Give the extent of all uninfected red blood cells.
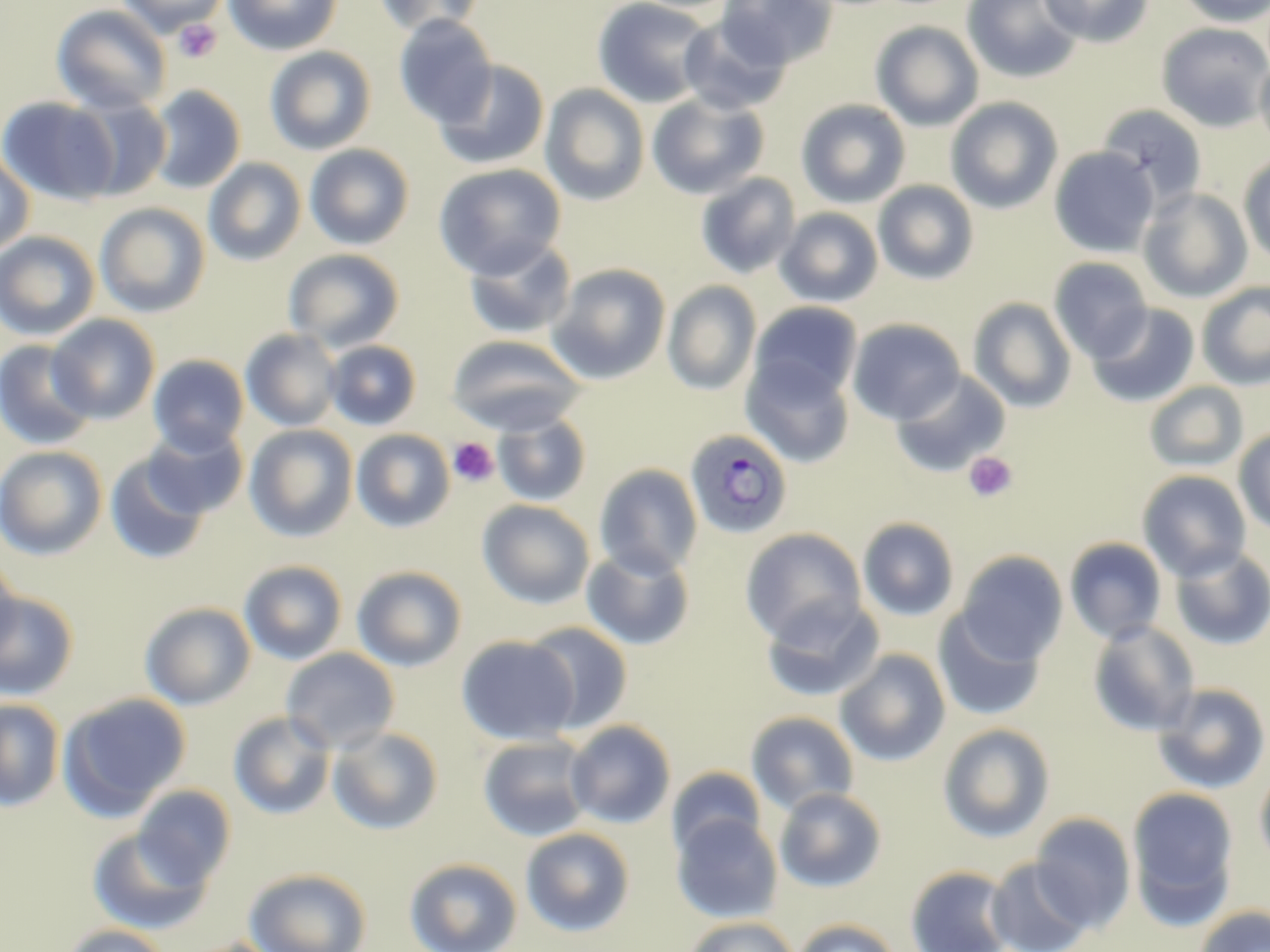
Approximate bounding boxes as named x1/y1/x2/y2 corners in pixels.
Uninfected red blood cells: (x1=115, y1=0, x2=229, y2=35), (x1=223, y1=0, x2=341, y2=56), (x1=373, y1=0, x2=486, y2=37), (x1=592, y1=0, x2=714, y2=109), (x1=717, y1=0, x2=837, y2=70), (x1=962, y1=0, x2=1083, y2=83), (x1=1039, y1=0, x2=1154, y2=47), (x1=1178, y1=0, x2=1270, y2=27), (x1=51, y1=4, x2=172, y2=115), (x1=393, y1=15, x2=498, y2=129), (x1=678, y1=17, x2=791, y2=115), (x1=871, y1=21, x2=984, y2=131), (x1=1156, y1=23, x2=1270, y2=131), (x1=264, y1=46, x2=376, y2=155), (x1=1255, y1=58, x2=1270, y2=154), (x1=433, y1=60, x2=550, y2=170), (x1=541, y1=84, x2=650, y2=206), (x1=148, y1=85, x2=245, y2=194), (x1=647, y1=93, x2=769, y2=200), (x1=0, y1=97, x2=121, y2=205), (x1=77, y1=97, x2=172, y2=200), (x1=945, y1=97, x2=1063, y2=214), (x1=795, y1=99, x2=911, y2=209), (x1=1096, y1=105, x2=1208, y2=208), (x1=304, y1=143, x2=415, y2=250), (x1=1050, y1=146, x2=1159, y2=258), (x1=0, y1=151, x2=35, y2=256), (x1=1238, y1=154, x2=1270, y2=265), (x1=203, y1=158, x2=306, y2=266), (x1=433, y1=163, x2=567, y2=279), (x1=695, y1=173, x2=801, y2=279), (x1=873, y1=180, x2=979, y2=285), (x1=1138, y1=188, x2=1253, y2=303), (x1=94, y1=202, x2=211, y2=318), (x1=775, y1=207, x2=883, y2=308), (x1=0, y1=231, x2=100, y2=340), (x1=463, y1=236, x2=576, y2=341), (x1=283, y1=249, x2=405, y2=352), (x1=1048, y1=257, x2=1152, y2=361), (x1=548, y1=264, x2=671, y2=384), (x1=663, y1=281, x2=761, y2=396), (x1=1197, y1=281, x2=1270, y2=389), (x1=968, y1=297, x2=1077, y2=413), (x1=748, y1=302, x2=863, y2=407), (x1=1087, y1=303, x2=1200, y2=408), (x1=47, y1=314, x2=160, y2=423), (x1=848, y1=318, x2=966, y2=425), (x1=241, y1=329, x2=343, y2=432), (x1=447, y1=335, x2=585, y2=434), (x1=1, y1=339, x2=97, y2=450), (x1=324, y1=340, x2=421, y2=430), (x1=148, y1=355, x2=249, y2=456), (x1=741, y1=358, x2=855, y2=468), (x1=890, y1=370, x2=1010, y2=477), (x1=1144, y1=381, x2=1248, y2=474), (x1=491, y1=409, x2=591, y2=507), (x1=141, y1=424, x2=249, y2=519), (x1=245, y1=424, x2=358, y2=543), (x1=1233, y1=428, x2=1270, y2=536), (x1=351, y1=429, x2=455, y2=533), (x1=0, y1=446, x2=107, y2=560), (x1=105, y1=451, x2=212, y2=565), (x1=594, y1=463, x2=703, y2=579), (x1=1137, y1=470, x2=1252, y2=581), (x1=477, y1=499, x2=595, y2=609), (x1=857, y1=517, x2=960, y2=621), (x1=739, y1=528, x2=867, y2=644), (x1=1064, y1=537, x2=1168, y2=645), (x1=1168, y1=544, x2=1270, y2=651), (x1=581, y1=547, x2=695, y2=650), (x1=954, y1=550, x2=1069, y2=666), (x1=0, y1=554, x2=20, y2=666), (x1=238, y1=560, x2=348, y2=665), (x1=351, y1=565, x2=468, y2=672), (x1=0, y1=591, x2=79, y2=701), (x1=761, y1=596, x2=884, y2=703), (x1=139, y1=602, x2=256, y2=710), (x1=933, y1=608, x2=1046, y2=721), (x1=1087, y1=620, x2=1201, y2=737), (x1=522, y1=622, x2=633, y2=733), (x1=456, y1=635, x2=579, y2=746), (x1=280, y1=648, x2=400, y2=753), (x1=834, y1=649, x2=951, y2=767), (x1=1152, y1=683, x2=1270, y2=794), (x1=57, y1=693, x2=191, y2=818), (x1=0, y1=699, x2=65, y2=812), (x1=745, y1=711, x2=860, y2=816), (x1=228, y1=712, x2=336, y2=820), (x1=564, y1=720, x2=676, y2=828), (x1=937, y1=723, x2=1055, y2=843), (x1=327, y1=726, x2=443, y2=835), (x1=478, y1=735, x2=593, y2=842), (x1=1254, y1=762, x2=1270, y2=873), (x1=667, y1=766, x2=767, y2=860), (x1=132, y1=786, x2=237, y2=890), (x1=1126, y1=786, x2=1239, y2=925), (x1=774, y1=787, x2=887, y2=892), (x1=1030, y1=812, x2=1136, y2=930), (x1=671, y1=813, x2=782, y2=923), (x1=87, y1=826, x2=215, y2=935), (x1=520, y1=827, x2=635, y2=937), (x1=404, y1=857, x2=523, y2=952), (x1=985, y1=857, x2=1093, y2=952), (x1=905, y1=865, x2=1015, y2=952), (x1=243, y1=867, x2=373, y2=952), (x1=1193, y1=905, x2=1270, y2=952), (x1=683, y1=916, x2=798, y2=952), (x1=793, y1=918, x2=901, y2=952), (x1=60, y1=924, x2=172, y2=952), (x1=178, y1=938, x2=288, y2=952).

Platelet locations: (x1=173, y1=19, x2=222, y2=63), (x1=448, y1=438, x2=499, y2=487), (x1=963, y1=451, x2=1018, y2=503). Plasmodium ovale-infected red blood cell locations: (x1=684, y1=428, x2=794, y2=540). Slide-level diagnosis: Plasmodium ovale. Light microscopy. Thin blood film. One field of a larger specimen. Captured at 1000x magnification. May-Grünwald-Giemsa stain. Image is 1270×952 pixels.